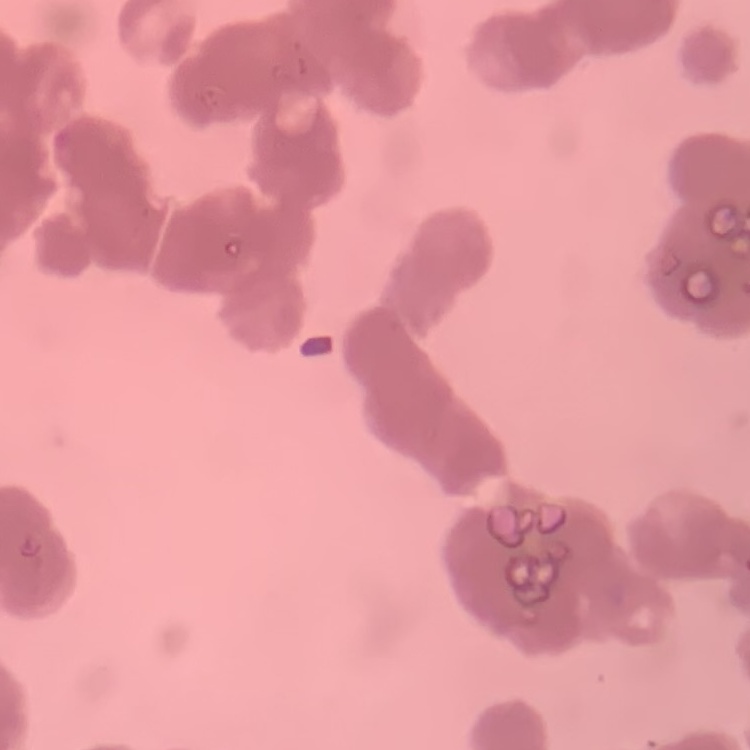
Summary:
  - Erythrocyte morphology: rouleaux formation
  - Image type: square crop of a larger photomicrograph
  - Stain: Field's or Giemsa
  - Preparation: thin blood film